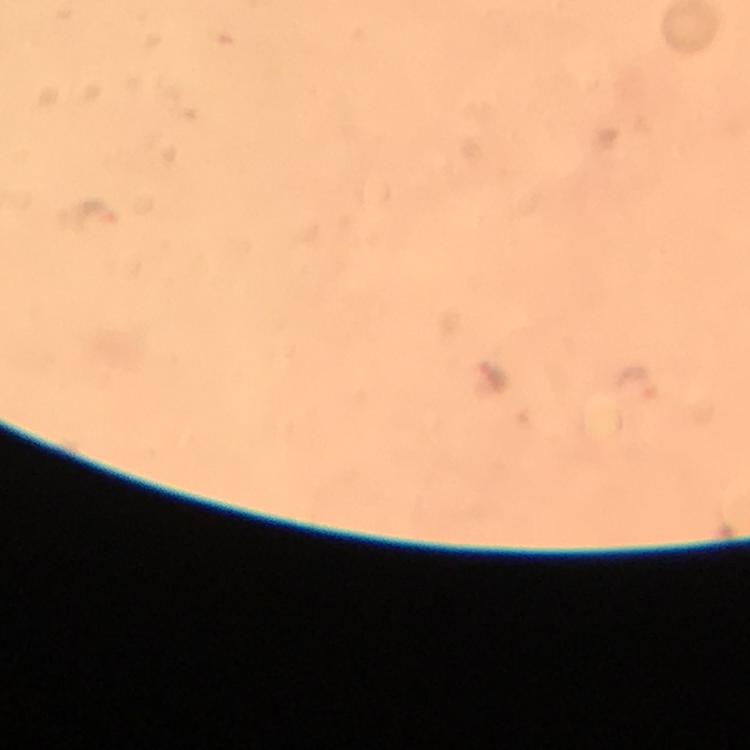

Approximate object centers, in pixels from the top-left corner.
Summary:
  - Plasmodium parasite locations: (x=97, y=214), (x=494, y=376), (x=638, y=386)
  - Context: from a diagnostic examination for malaria
  - Capture: smartphone camera through the microscope
  - Stain: Giemsa
  - Cropped from: one field of view
  - Magnification: 100x
  - Preparation: thick blood film
  - Immersion oil: applied
  - Image size: 750×750 pixels